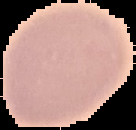

{
  "result": "negative for malaria parasites",
  "image_type": "segmented cell region on a black background",
  "preparation": "thin blood smear",
  "image_size": "136×130 pixels"
}